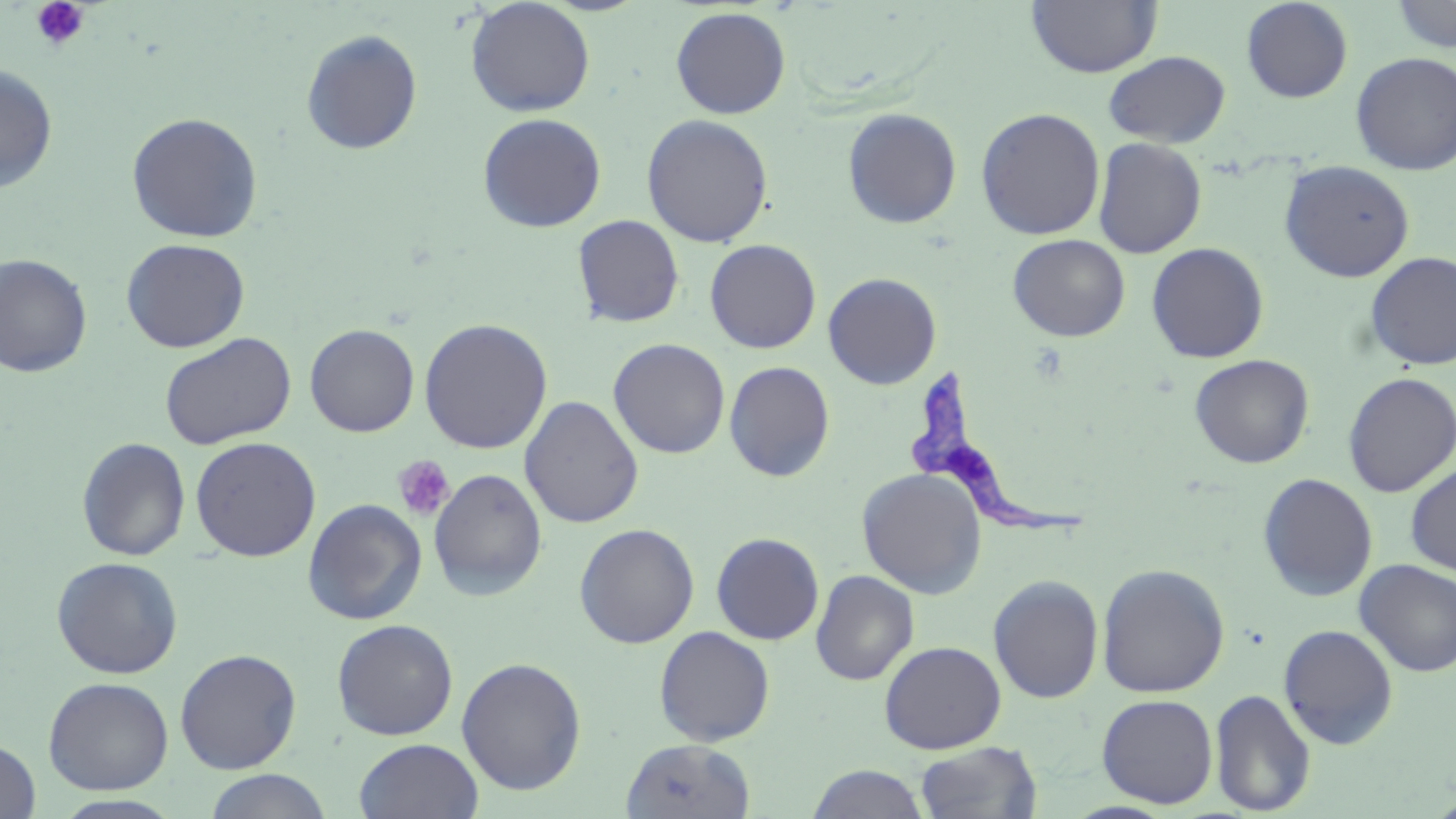 Approximate bounding boxes as (x1, y1, x2, y2) in pixels. Uninfected red blood cell locations: (465, 0, 595, 117), (1027, 0, 1161, 77), (1241, 0, 1353, 103), (1389, 0, 1455, 53), (670, 6, 791, 119), (300, 28, 423, 155), (1103, 50, 1231, 147), (1351, 52, 1456, 176), (0, 64, 58, 194), (842, 107, 962, 229), (976, 107, 1105, 240), (126, 112, 264, 243), (478, 113, 607, 232), (641, 114, 774, 247), (1092, 138, 1207, 258), (1279, 159, 1415, 282), (572, 215, 685, 328), (1008, 234, 1130, 341), (120, 237, 250, 353), (704, 239, 821, 354), (1146, 242, 1269, 364), (1364, 251, 1456, 371), (0, 253, 93, 378), (822, 272, 942, 390), (419, 318, 553, 454), (304, 324, 420, 437), (160, 332, 296, 450), (608, 338, 730, 459), (1190, 353, 1314, 468), (724, 361, 835, 482), (1342, 372, 1455, 497), (519, 395, 644, 528), (190, 436, 321, 562), (76, 437, 191, 561), (1405, 462, 1456, 576), (428, 468, 548, 601), (857, 468, 987, 599), (1257, 472, 1378, 601), (302, 499, 427, 625), (574, 523, 699, 649), (711, 532, 825, 645), (51, 556, 184, 679), (1355, 559, 1456, 676), (1096, 563, 1230, 698), (810, 569, 919, 686), (987, 574, 1105, 704), (331, 619, 458, 740), (1278, 624, 1399, 749), (653, 626, 775, 746), (879, 640, 1006, 754), (174, 648, 302, 774), (456, 657, 588, 795), (43, 677, 174, 794), (1209, 688, 1316, 815), (1096, 693, 1219, 808), (354, 737, 484, 819), (620, 738, 756, 818), (0, 739, 41, 818), (914, 741, 1043, 819), (806, 764, 930, 819), (203, 769, 333, 819), (52, 794, 185, 818). Platelet locations: (31, 0, 90, 52), (392, 455, 455, 522). Trypanosoma brucei locations: (911, 372, 1084, 537). Slide-level diagnosis: Trypanosoma brucei. Thin blood smear. Captured at 1000x magnification. Light microscopy. Image is 1456×819 pixels. One field of a larger specimen. May-Grünwald-Giemsa stain.